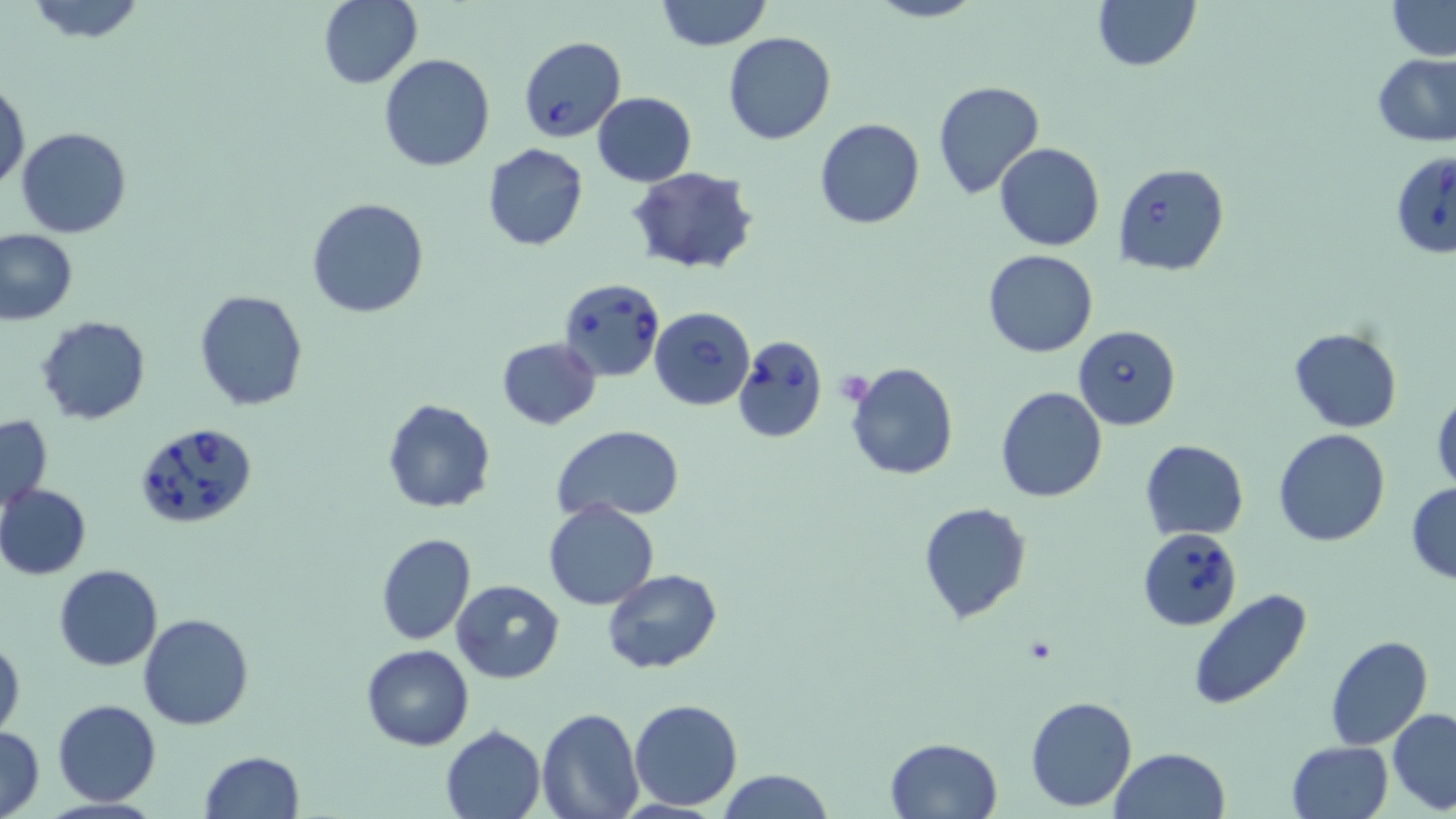

slide-level diagnosis = Babesia divergens
platelet locations = approximate bounding boxes as named x1/y1/x2/y2 corners in pixels: (x1=840, y1=373, x2=874, y2=401)
stain = May-Grünwald-Giemsa
image size = 1456×819 pixels
Babesia divergens-infected red blood cell locations = approximate bounding boxes as named x1/y1/x2/y2 corners in pixels: (x1=518, y1=35, x2=625, y2=141), (x1=1392, y1=152, x2=1456, y2=257), (x1=1113, y1=162, x2=1230, y2=275), (x1=556, y1=276, x2=664, y2=383), (x1=649, y1=307, x2=756, y2=410), (x1=1072, y1=324, x2=1180, y2=430), (x1=733, y1=335, x2=829, y2=442), (x1=131, y1=422, x2=258, y2=530), (x1=1137, y1=527, x2=1242, y2=630)
magnification = 1000x
preparation = thin blood film
modality = light microscopy
uninfected red blood cell locations = approximate bounding boxes as named x1/y1/x2/y2 corners in pixels: (x1=23, y1=0, x2=147, y2=44), (x1=657, y1=0, x2=770, y2=51), (x1=866, y1=0, x2=985, y2=23), (x1=1092, y1=0, x2=1200, y2=71), (x1=1385, y1=0, x2=1455, y2=59), (x1=317, y1=1, x2=421, y2=88), (x1=723, y1=31, x2=836, y2=144), (x1=1373, y1=53, x2=1455, y2=146), (x1=378, y1=54, x2=495, y2=172), (x1=1, y1=78, x2=28, y2=192), (x1=933, y1=82, x2=1044, y2=200), (x1=592, y1=91, x2=696, y2=186), (x1=814, y1=119, x2=924, y2=229), (x1=16, y1=128, x2=131, y2=239), (x1=484, y1=143, x2=588, y2=252), (x1=995, y1=143, x2=1105, y2=252), (x1=625, y1=165, x2=759, y2=276), (x1=306, y1=197, x2=430, y2=318), (x1=0, y1=229, x2=77, y2=325), (x1=982, y1=250, x2=1099, y2=357), (x1=195, y1=290, x2=308, y2=410), (x1=37, y1=315, x2=150, y2=424), (x1=1288, y1=327, x2=1401, y2=433), (x1=496, y1=338, x2=601, y2=429), (x1=845, y1=361, x2=959, y2=480), (x1=995, y1=385, x2=1107, y2=503), (x1=1432, y1=389, x2=1456, y2=496), (x1=383, y1=399, x2=496, y2=514), (x1=0, y1=414, x2=52, y2=513), (x1=552, y1=425, x2=684, y2=524), (x1=1273, y1=428, x2=1392, y2=546), (x1=1139, y1=439, x2=1250, y2=539), (x1=0, y1=483, x2=92, y2=581), (x1=1406, y1=483, x2=1456, y2=583), (x1=542, y1=499, x2=660, y2=610), (x1=917, y1=502, x2=1031, y2=623), (x1=375, y1=532, x2=476, y2=646), (x1=52, y1=564, x2=163, y2=672), (x1=602, y1=568, x2=723, y2=673), (x1=450, y1=579, x2=565, y2=684), (x1=1189, y1=589, x2=1314, y2=712), (x1=138, y1=612, x2=254, y2=730), (x1=0, y1=633, x2=24, y2=739), (x1=1324, y1=635, x2=1433, y2=750), (x1=360, y1=643, x2=475, y2=750), (x1=1025, y1=695, x2=1137, y2=811), (x1=629, y1=698, x2=742, y2=811), (x1=52, y1=699, x2=160, y2=805), (x1=536, y1=706, x2=644, y2=819), (x1=1389, y1=708, x2=1456, y2=813), (x1=441, y1=725, x2=546, y2=818), (x1=1, y1=726, x2=43, y2=819), (x1=885, y1=737, x2=1003, y2=819), (x1=1285, y1=741, x2=1394, y2=819), (x1=1109, y1=747, x2=1231, y2=819), (x1=200, y1=750, x2=305, y2=818), (x1=715, y1=770, x2=835, y2=819)
field of view = one of a larger specimen